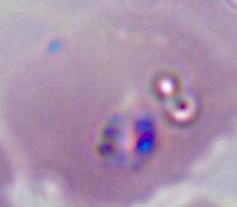

Summary:
  - Magnification: 400x or 1000x
  - Identification: Plasmodium
  - Modality: micrograph